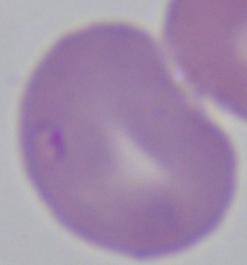

Photomicrograph. 1000x magnification. A Babesia parasite is shown.